Locate every malaria parasite.
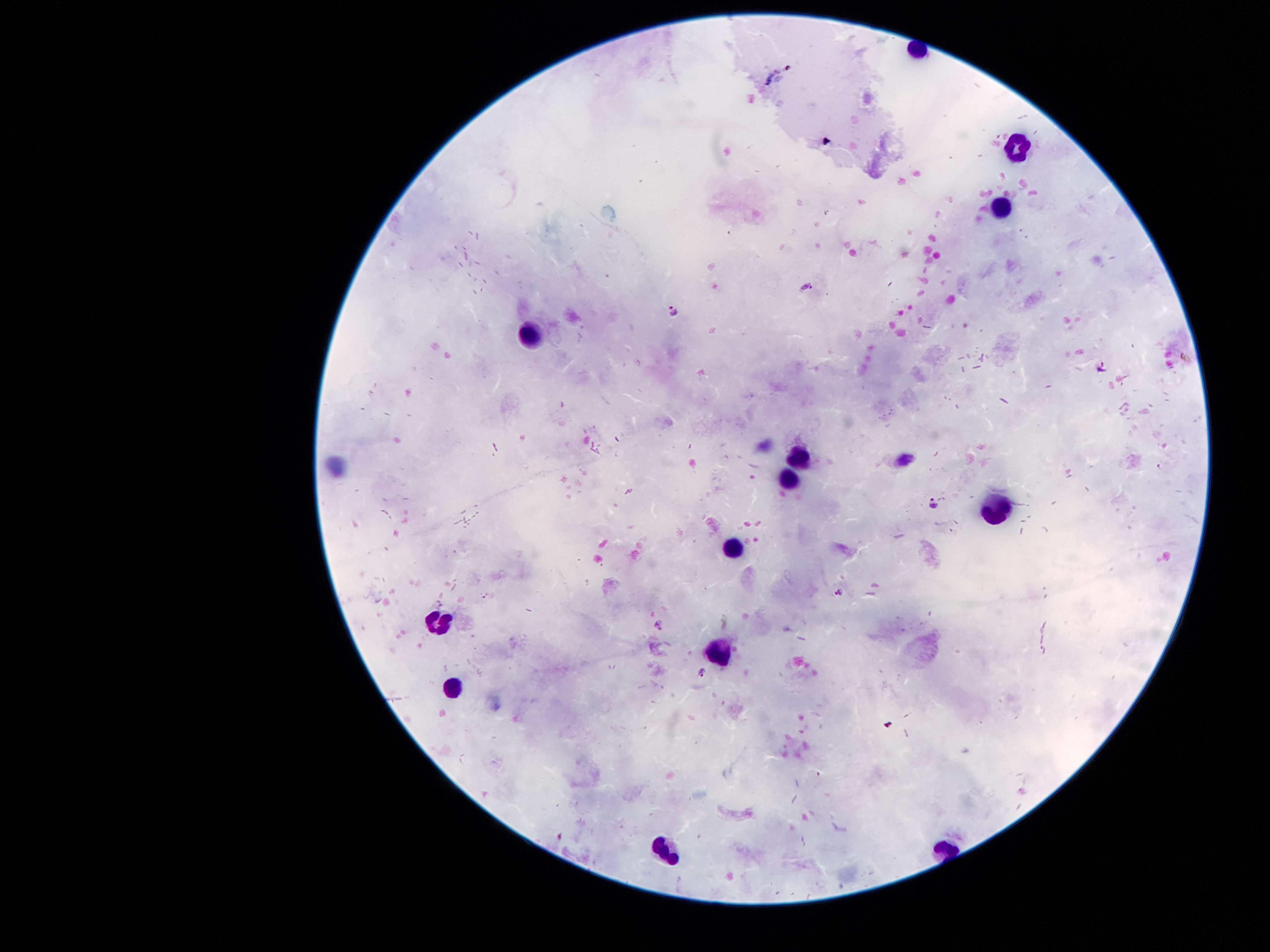

Approximate centers as (x, y) in pixels.
Malaria parasites: (808, 290), (673, 310), (1104, 370), (934, 504), (838, 591), (701, 672).

Summary:
  - Leukocyte locations: (1018, 144), (1005, 202), (530, 330), (798, 456), (788, 477), (998, 511), (730, 547), (439, 624), (717, 651), (456, 687), (659, 852)
  - Stain: Giemsa
  - Capture: smartphone through the microscope eyepiece
  - Magnification: 100x
  - Field of view: one from this slide
  - Patient malaria status: positive for Plasmodium falciparum
  - Image size: 1270×952 pixels
  - Preparation: thick peripheral-blood smear